Point out each Plasmodium parasite.
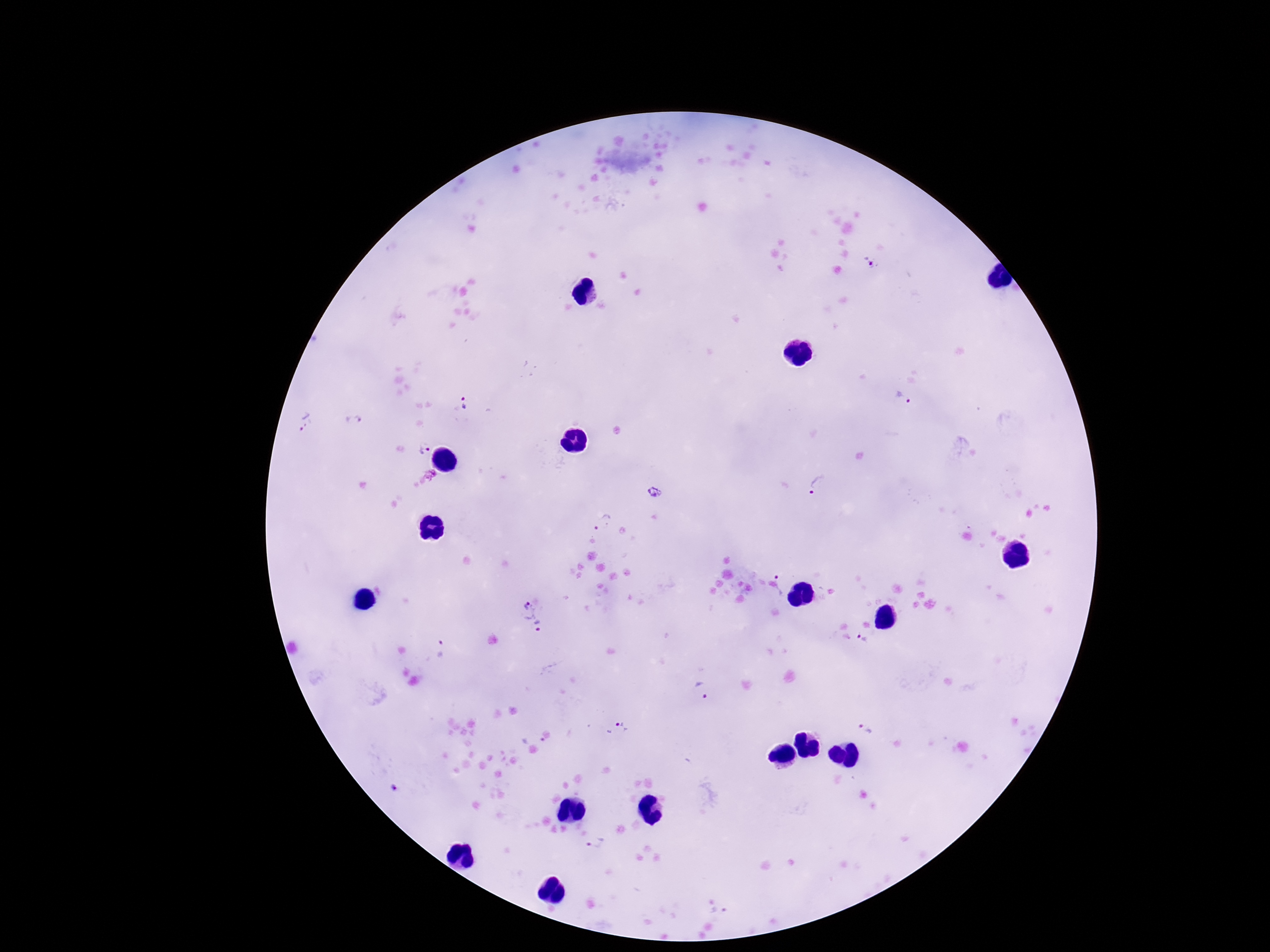
Approximate object centers, in pixels from the top-left corner.
Plasmodium parasites: (x=871, y=262), (x=904, y=399), (x=464, y=405), (x=306, y=421), (x=353, y=423), (x=421, y=448), (x=818, y=484), (x=654, y=492), (x=604, y=523), (x=786, y=577), (x=532, y=615), (x=863, y=638), (x=440, y=649), (x=699, y=691), (x=620, y=726), (x=868, y=728), (x=594, y=844).

field of view = one from this slide
image size = 1270×952 pixels
magnification = 100x
patient malaria status = positive
preparation = thick blood smear
capture = smartphone camera through the microscope eyepiece
stain = Giemsa